Name the parasite shown.
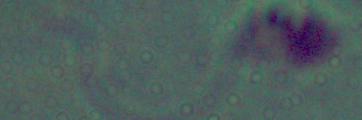

Leishmania.

1000x magnification. Micrograph.